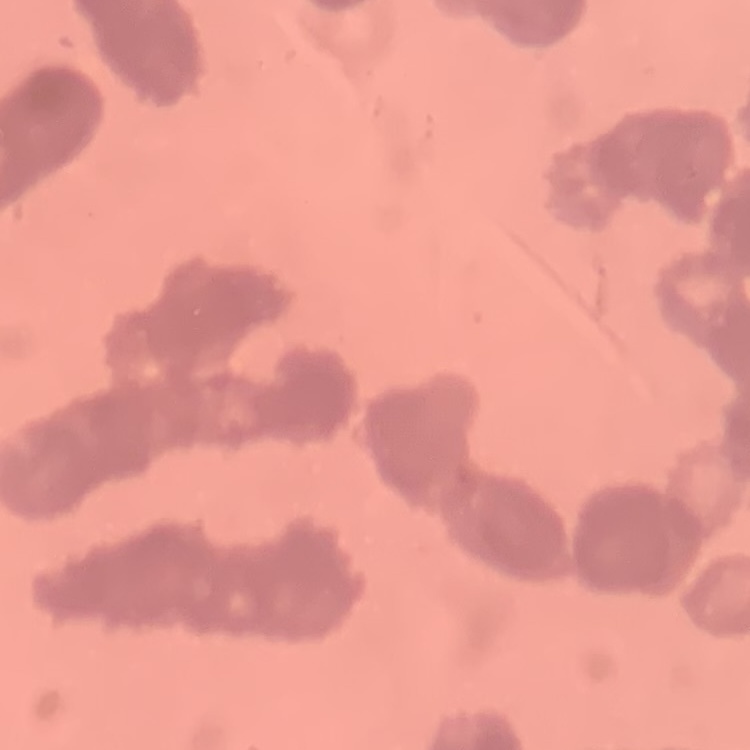

The red blood cells exhibit rouleaux formation. Thin peripheral smear. One tile cut from a larger photomicrograph. Field's or Giemsa stain.